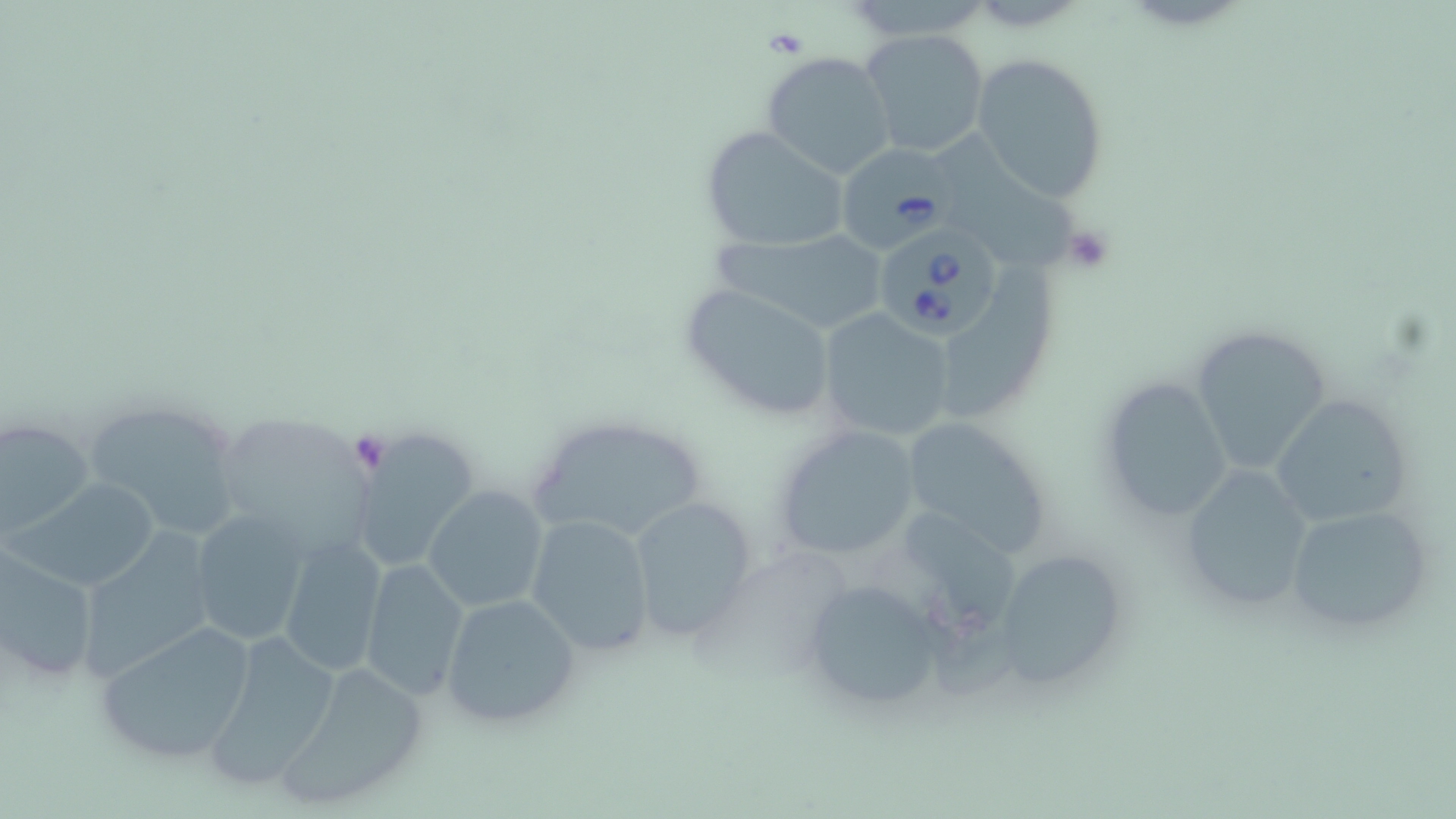
{
  "slide_level_diagnosis": "Babesia divergens",
  "modality": "light microscopy",
  "platelet_locations": "approximate bounding boxes as [x1, y1, x2, y2] in pixels: [762, 26, 809, 60], [1058, 224, 1115, 275], [347, 432, 394, 473]",
  "uninfected_red_blood_cell_locations": "approximate bounding boxes as [x1, y1, x2, y2] in pixels: [860, 28, 991, 159], [759, 50, 897, 180], [971, 51, 1110, 205], [699, 125, 851, 254], [938, 132, 1075, 271], [707, 223, 888, 335], [948, 263, 1064, 420], [676, 281, 842, 425], [815, 307, 958, 441], [1191, 321, 1335, 474], [1094, 377, 1232, 521], [1267, 393, 1411, 527], [80, 396, 250, 540], [527, 413, 711, 543], [208, 415, 379, 569], [0, 416, 94, 537], [896, 416, 1058, 563], [770, 420, 926, 563], [348, 426, 479, 573], [1173, 467, 1318, 617], [13, 477, 162, 591], [422, 487, 549, 612], [625, 495, 760, 642], [1280, 503, 1437, 634], [897, 507, 1026, 640], [188, 508, 311, 648], [524, 513, 657, 658], [75, 528, 219, 681], [279, 534, 387, 676], [994, 548, 1131, 683], [1, 549, 99, 686], [360, 557, 468, 700], [797, 574, 950, 719], [439, 593, 582, 729], [92, 621, 258, 766], [200, 627, 346, 791], [272, 660, 434, 811]",
  "preparation": "thin blood film",
  "stain": "May-Grünwald-Giemsa",
  "field_of_view": "one of a larger specimen",
  "image_size": "1456×819 pixels",
  "magnification": "1000x",
  "babesia_divergens_infected_red_blood_cell_locations": "approximate bounding boxes as [x1, y1, x2, y2] in pixels: [836, 146, 957, 254], [872, 222, 1003, 338]"
}